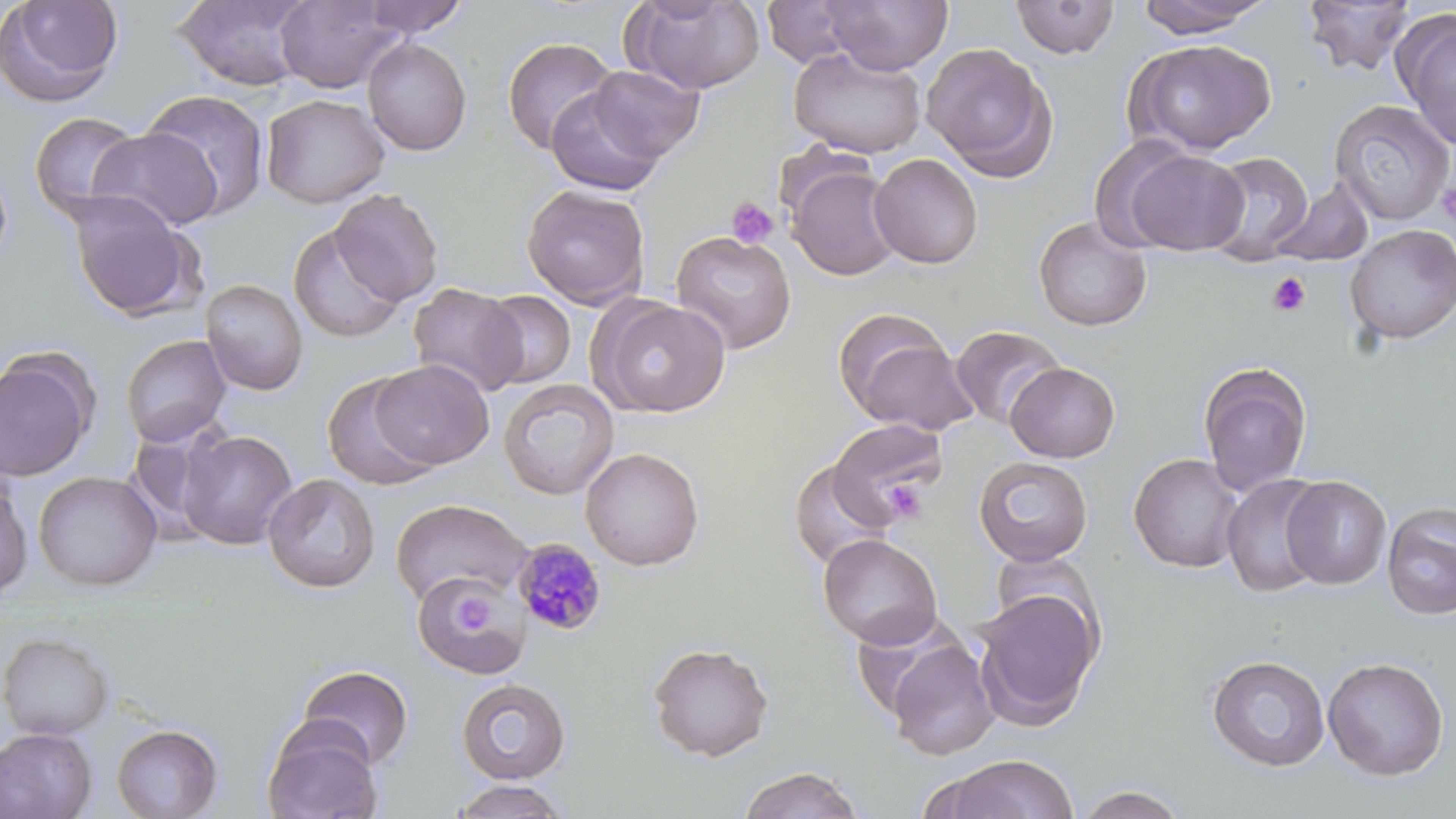

Plasmodium malariae-infected red blood cell locations = approximate bounding boxes as (x1, y1, x2, y2) in pixels: (511, 537, 608, 636)
slide-level diagnosis = Plasmodium malariae
image size = 1456×819 pixels
stain = May-Grünwald-Giemsa
uninfected red blood cell locations = approximate bounding boxes as (x1, y1, x2, y2) in pixels: (173, 0, 316, 91), (358, 0, 470, 39), (821, 0, 953, 75), (1010, 0, 1121, 59), (1136, 0, 1274, 38), (1300, 0, 1418, 76), (1, 1, 125, 107), (275, 1, 403, 93), (626, 1, 765, 95), (761, 1, 870, 70), (1393, 10, 1456, 151), (501, 36, 620, 155), (361, 37, 473, 156), (1130, 38, 1277, 154), (921, 42, 1057, 180), (788, 45, 926, 159), (587, 64, 706, 161), (545, 87, 664, 196), (140, 88, 272, 221), (261, 94, 390, 209), (1328, 99, 1455, 226), (29, 111, 143, 224), (87, 127, 225, 232), (1118, 147, 1249, 255), (869, 153, 983, 269), (1202, 153, 1312, 265), (784, 161, 904, 281), (1270, 178, 1374, 267), (522, 185, 650, 308), (329, 189, 444, 305), (66, 191, 202, 322), (1033, 216, 1153, 332), (287, 224, 406, 344), (1344, 224, 1456, 345), (671, 230, 797, 354), (200, 278, 308, 395), (407, 283, 527, 397), (476, 290, 577, 389), (595, 297, 731, 417), (835, 315, 976, 436), (950, 324, 1066, 430), (120, 334, 232, 447), (0, 351, 97, 482), (369, 359, 494, 470), (1197, 361, 1313, 495), (1005, 362, 1120, 463), (323, 373, 439, 490), (498, 378, 619, 500), (827, 418, 948, 526), (122, 420, 238, 546), (178, 429, 298, 549), (580, 447, 705, 571), (1128, 453, 1246, 573), (973, 456, 1093, 567), (789, 459, 895, 571), (33, 470, 162, 591), (262, 473, 380, 593), (1221, 474, 1331, 597), (0, 476, 34, 600), (1280, 476, 1391, 589), (390, 498, 533, 607), (1381, 503, 1456, 619), (817, 533, 942, 648), (413, 572, 530, 678), (971, 589, 1102, 728), (887, 619, 1097, 748), (0, 631, 115, 741), (887, 639, 999, 760), (647, 642, 775, 761), (1206, 654, 1330, 772), (1322, 657, 1448, 780), (297, 665, 414, 771), (456, 678, 571, 784), (262, 722, 382, 819), (111, 724, 223, 818), (0, 728, 98, 819), (932, 753, 1079, 818), (739, 766, 864, 818), (447, 780, 571, 819), (1072, 785, 1192, 819)
platelet locations = approximate bounding boxes as (x1, y1, x2, y2) in pixels: (1436, 180, 1456, 230), (726, 196, 780, 249), (1267, 272, 1311, 317), (884, 479, 929, 523), (448, 589, 494, 638)
preparation = thin blood film
modality = light microscopy
magnification = 1000x
field of view = single